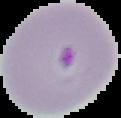
Segmented cell region on a black background. Image is 121×118 pixels. Result: Plasmodium parasites detected. From a thin blood film.